Assess the morphology of the red blood cells.
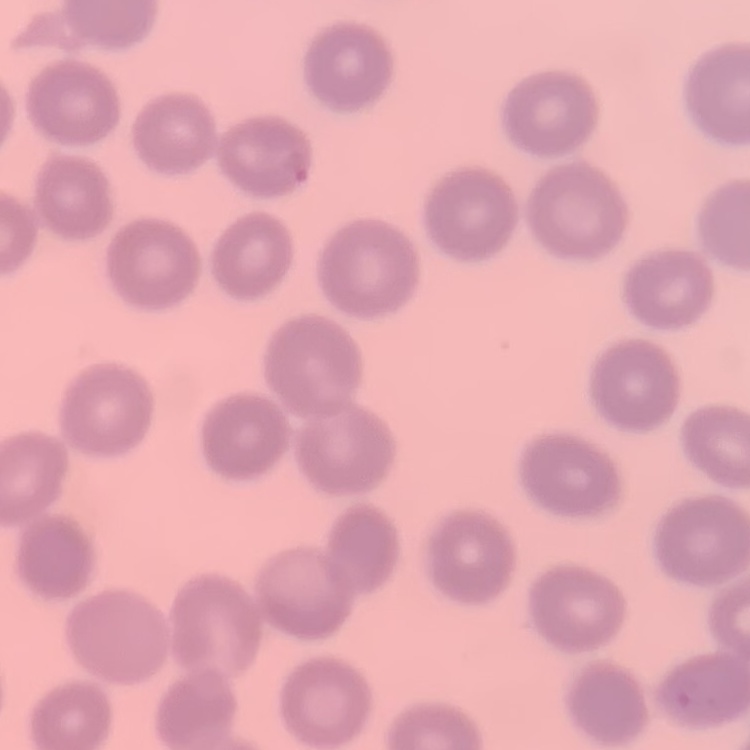

They show no rouleaux formation.

Stained with either Field's or Giemsa. Square crop of a larger photomicrograph. Thin blood film.